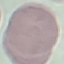

malaria status = uninfected
image type = automatically extracted cell patch, resized to 64 × 64 pixels
capture = smartphone through the microscope eyepiece
preparation = thin blood smear
stain = Giemsa